Assess for malaria.
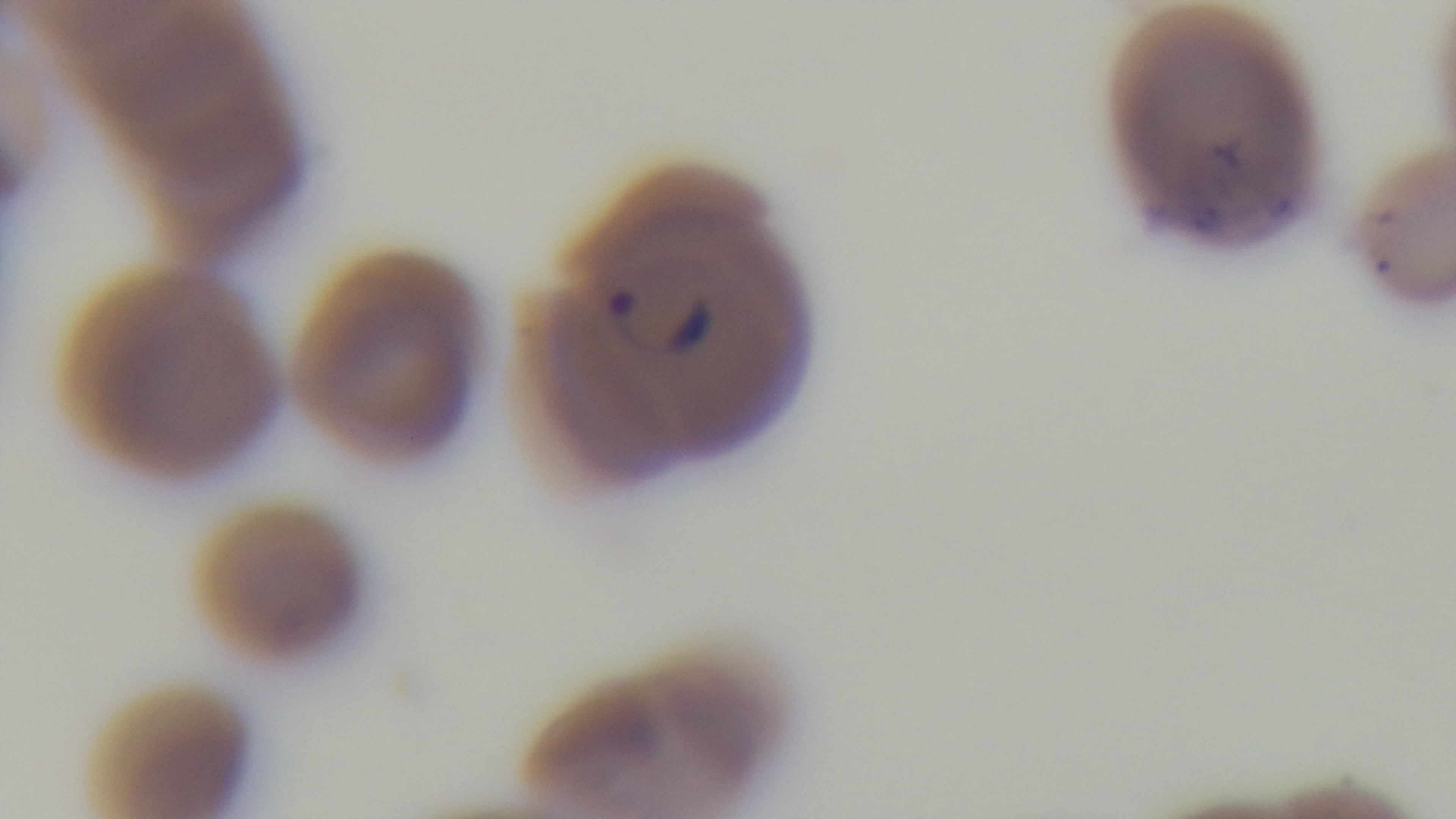

Positive.

Summary:
  - Objective: 100x oil immersion
  - Stain: Giemsa
  - Preparation: thin smear
  - Capture: mounted 4K digital camera
  - Field of view: single
  - Modality: light microscopy